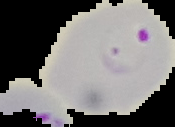
Malaria status: parasitized. From a thin blood smear. Segmented cell region on a black background. Image is 175×127 pixels.